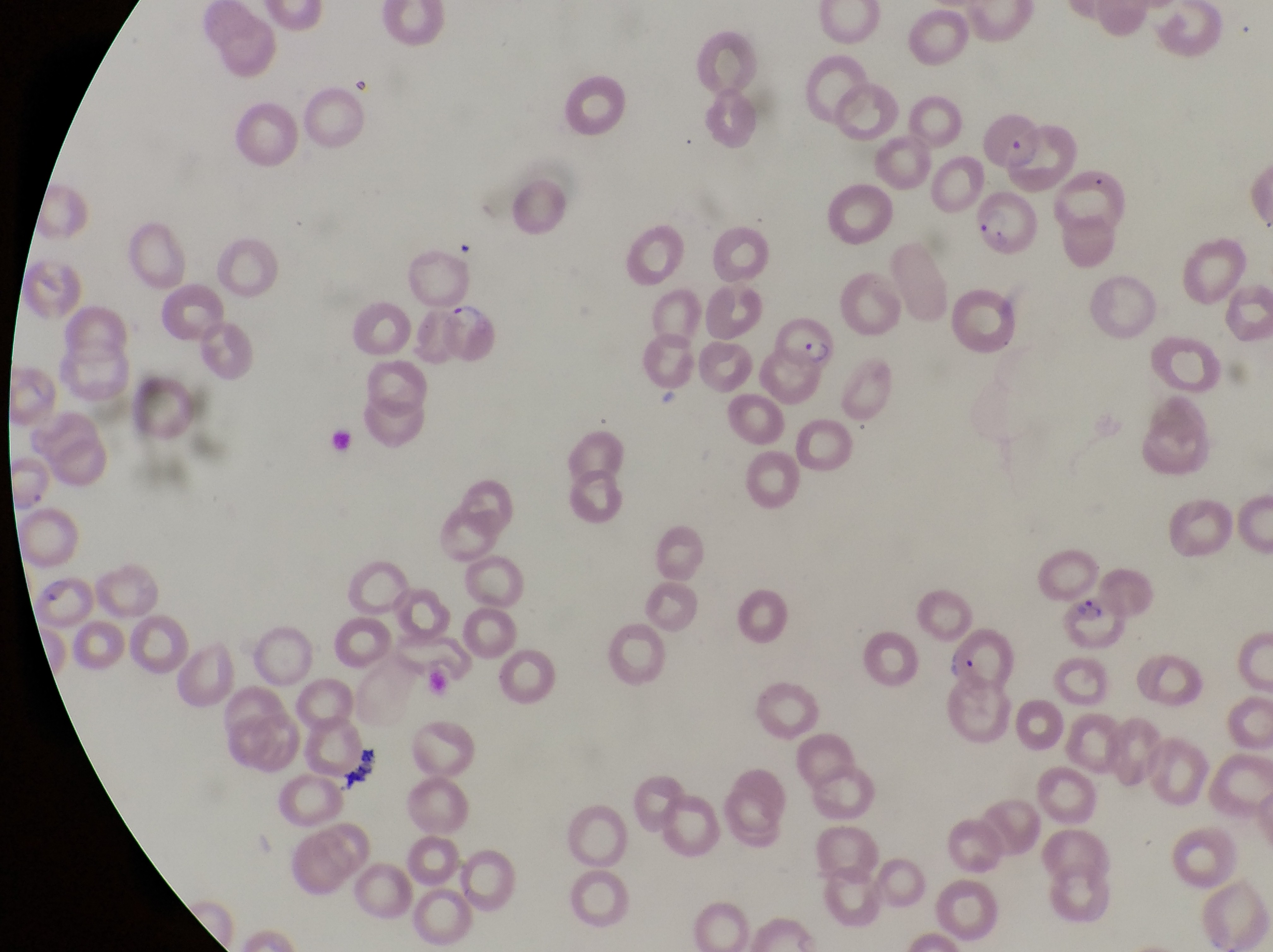 Approximate bounding boxes as {left, top, right, bottom} in pixels. Parasitised red blood cell locations: {981, 115, 1043, 165}, {1058, 165, 1129, 231}, {978, 190, 1043, 264}, {445, 304, 500, 366}, {778, 312, 847, 375}, {3, 456, 58, 509}, {29, 570, 92, 625}, {1060, 596, 1129, 651}, {944, 629, 1015, 687}. Collected in Uganda. Captured by a smartphone held over the eyepiece of an Olympus CX-23 microscope. Magnification of 1000x. Single field of view. Image is 1273×952 pixels. Thin blood film.